Describe the morphology of the red blood cells.
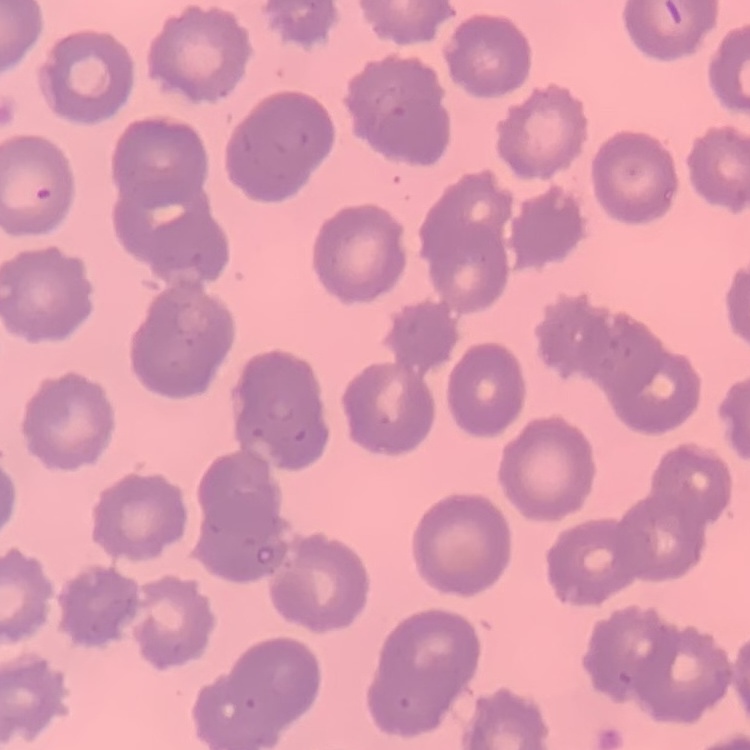

They show no rouleaux formation.

stain = Field's or Giemsa
image type = square crop of a larger photomicrograph
preparation = thin blood film